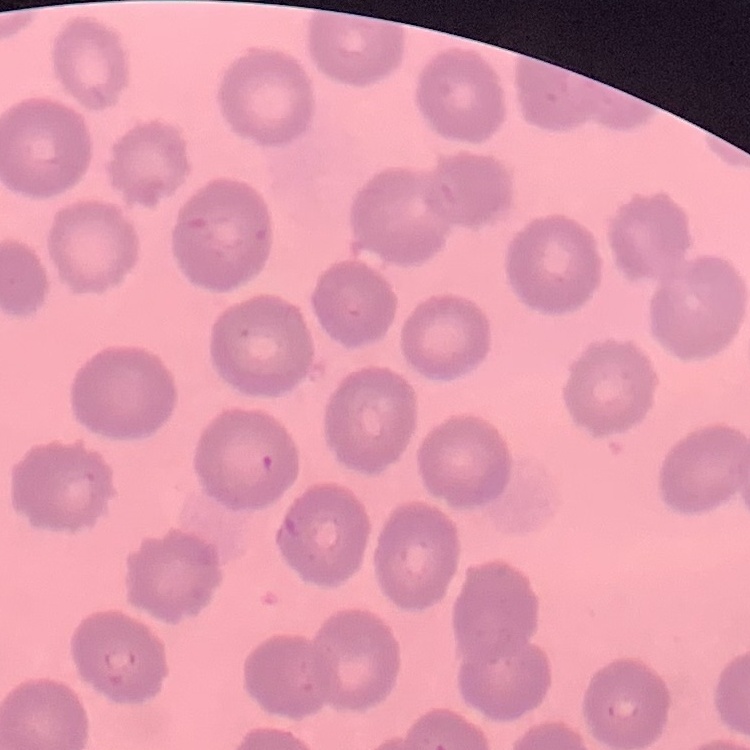
Summary:
  - Erythrocyte morphology: no rouleaux formation
  - Preparation: thin blood film
  - Stain: Field's or Giemsa
  - Image type: square crop of a larger photomicrograph